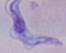

Summary:
  - Modality: photomicrograph
  - Identification: trypanosome
  - Magnification: 1000x